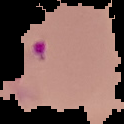

Summary:
  - Malaria status: parasitized
  - Image size: 124×124 pixels
  - Image type: cell region segmented out of the field of view; surrounding area masked to black
  - Preparation: thin blood film